Locate and identify every blood parasite.
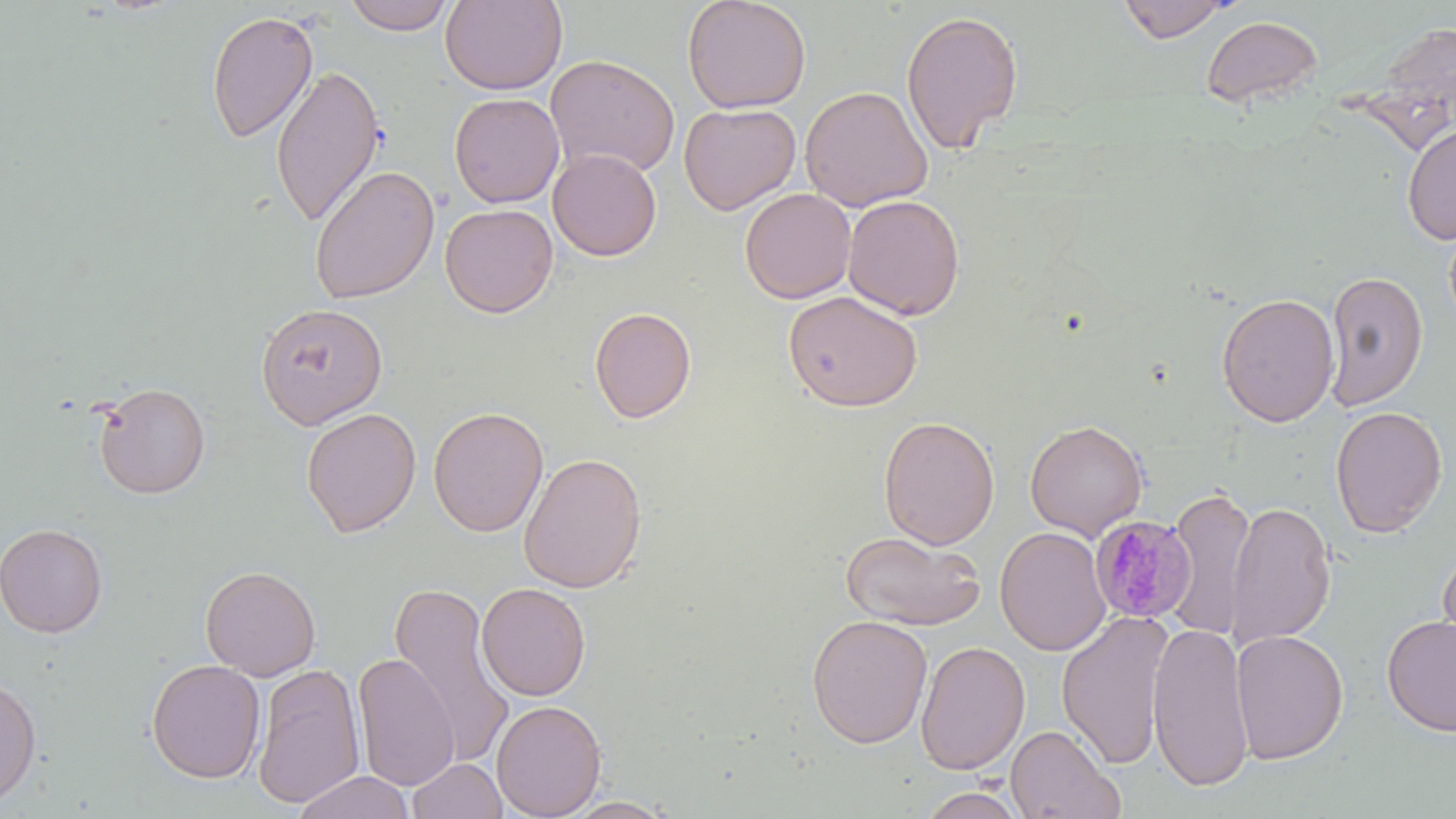
Approximate bounding boxes as (x1, y1, x2, y2) in pixels.
Plasmodium malariae-infected red blood cells: (1089, 515, 1197, 624).
No Plasmodium falciparum, Plasmodium ovale, Plasmodium vivax, Babesia divergens, or Trypanosoma brucei observed.

slide_level_diagnosis: Plasmodium malariae
field_of_view: one of a larger specimen
modality: optical microscopy
preparation: thin blood smear
image_size: 1456×819 pixels
stain: May-Grünwald-Giemsa
uninfected_red_blood_cell_locations: 'approximate bounding boxes as (x1, y1, x2, y2) in pixels: (343, 0, 455, 35), (682, 0, 811, 114), (1118, 0, 1232, 42), (439, 1, 568, 95), (901, 8, 1023, 155), (206, 9, 319, 145), (1201, 15, 1323, 108), (545, 54, 680, 180), (270, 64, 386, 229), (799, 86, 933, 213), (448, 92, 564, 208), (679, 103, 801, 215), (1401, 122, 1456, 246), (547, 148, 662, 261), (308, 164, 440, 304), (739, 188, 856, 303), (842, 194, 965, 320), (439, 203, 559, 318), (1323, 270, 1428, 412), (783, 289, 923, 412), (1215, 293, 1340, 427), (255, 303, 388, 429), (589, 306, 697, 423), (93, 382, 211, 498), (1330, 405, 1448, 537), (301, 406, 421, 537), (428, 406, 548, 537), (878, 415, 1000, 550), (1025, 420, 1148, 540), (518, 452, 647, 593), (1167, 486, 1256, 641), (1226, 501, 1336, 647), (0, 521, 108, 638), (995, 527, 1111, 656), (839, 531, 986, 630), (1436, 540, 1456, 661), (199, 564, 321, 681), (387, 580, 517, 767), (476, 582, 592, 701), (1056, 610, 1173, 769), (806, 614, 932, 749), (1381, 615, 1456, 737), (1147, 621, 1255, 792), (1230, 629, 1348, 764), (915, 640, 1031, 775), (352, 652, 460, 791), (146, 659, 266, 784), (251, 662, 365, 809), (0, 676, 42, 810), (491, 699, 607, 819), (1005, 724, 1124, 819), (407, 757, 508, 819), (291, 770, 415, 819), (916, 787, 1030, 818), (559, 795, 679, 818)'
magnification: 1000x